Give the position of every Plasmodium parasite.
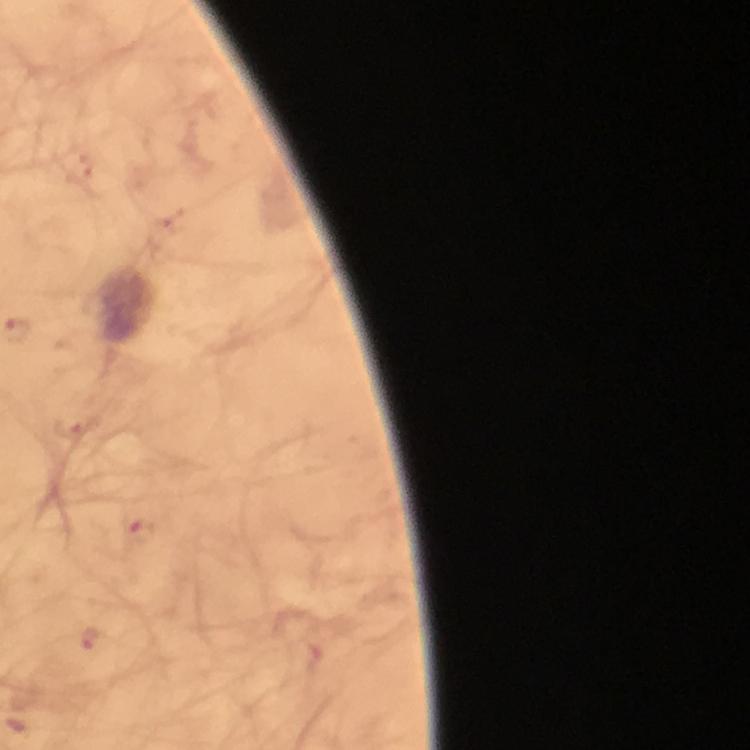

Approximate centers as {x, y} in pixels.
Plasmodium parasites: {70, 428}, {139, 529}, {93, 637}, {315, 657}.

Summary:
  - Context: from a diagnostic examination for malaria
  - Image size: 750×750 pixels
  - Immersion oil: used
  - Capture: smartphone mounted on the microscope
  - Stain: Giemsa
  - Preparation: thick smear
  - Cropped from: one field of view
  - Magnification: 100x